Assess this cell for malaria.
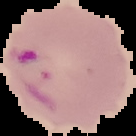

It is parasitized.

Image is 136×136 pixels. The area outside the segmented cell region is set to black. From a thin blood smear.